Comment on the morphology of the erythrocytes.
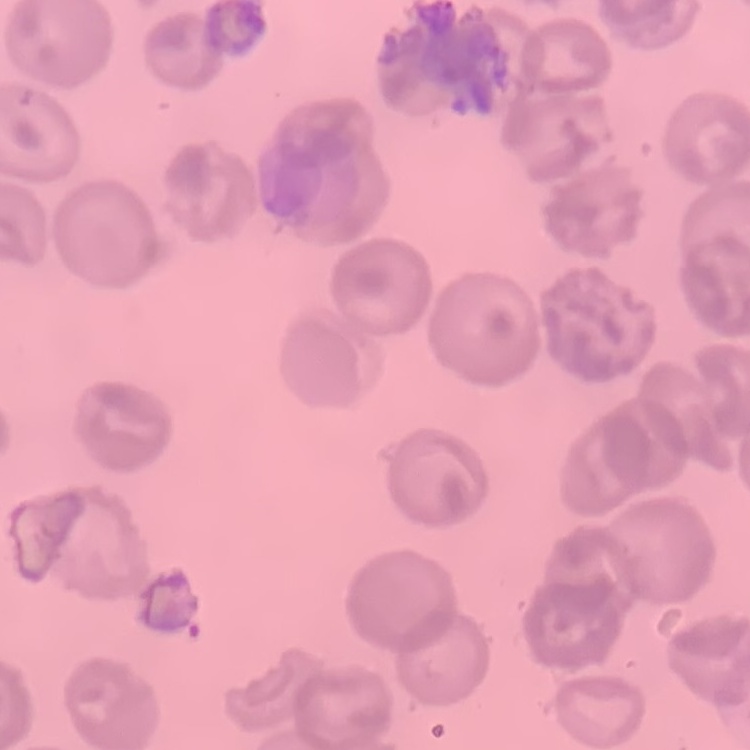

They show no rouleaux formation.

Summary:
  - Stain: Field's or Giemsa
  - Image type: one tile cut from a larger photomicrograph
  - Preparation: thin blood smear